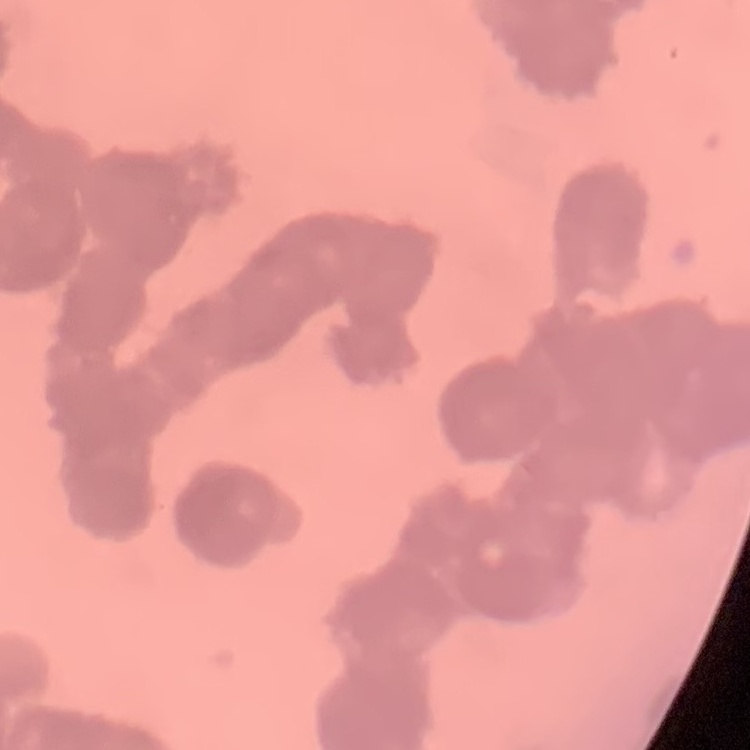

{
  "red_blood_cell_morphology": "rouleaux formation",
  "preparation": "thin blood film",
  "image_type": "one tile cut from a larger photomicrograph",
  "stain": "Field's or Giemsa"
}